Classify this cell by malaria status.
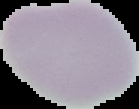
Uninfected.

{
  "image_size": "139×109 pixels",
  "preparation": "thin blood film",
  "image_type": "segmented cell region with the area outside set to black"
}